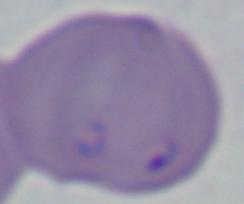 Micrograph. 1000x magnification. A Babesia parasite is shown.